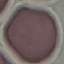 Malaria status: uninfected. Automatically extracted cell patch, resized to 64 × 64 pixels. Photographed with a smartphone camera at the microscope eyepiece. Giemsa-stained preparation. Thin smear of blood.